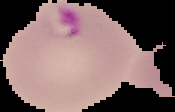
result: malaria parasites detected
image_size: 175×112 pixels
image_type: segmented cell region on a black background
preparation: thin blood film